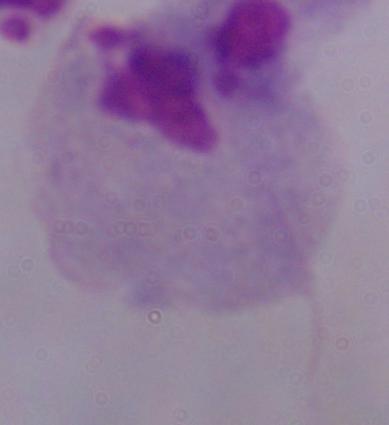

magnification = 1000x
identification = trichomonad
modality = micrograph